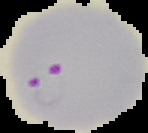

From a thin blood smear. Result: malaria parasites detected. Image is 148×133 pixels. The area outside the segmented cell region is set to black.